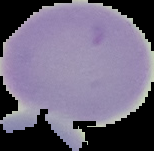
Summary:
  - Image type: segmented cell region on a black background
  - Malaria status: uninfected
  - Image size: 154×151 pixels
  - Preparation: thin blood smear